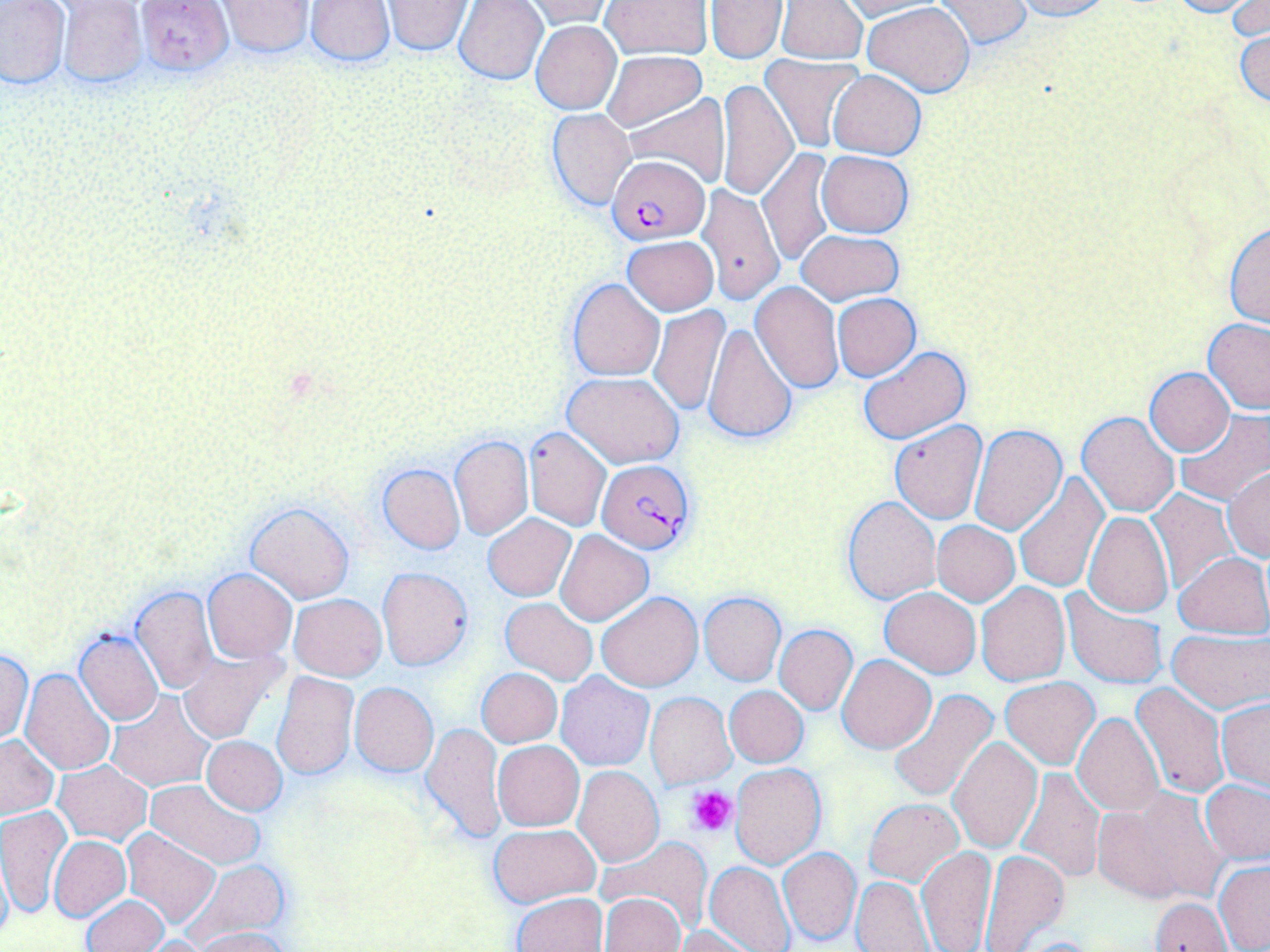
Summary:
  - Coordinate format: approximate bounding boxes as (x1,y1)-(x2,y2) corner pairs in pixels
  - Platelet locations: (688,785)-(739,837)
  - Plasmodium falciparum-infected red blood cell locations: (607,154)-(711,244), (596,458)-(697,555)
  - Uninfected red blood cell locations: (133,0)-(233,76), (304,0)-(395,67), (382,0)-(473,55), (518,0)-(615,29), (600,0)-(713,58), (706,0)-(786,63), (777,0)-(867,65), (1007,0)-(1111,21), (1165,0)-(1259,17), (1230,0)-(1269,42), (0,1)-(71,89), (57,1)-(149,88), (216,1)-(315,57), (454,1)-(549,85), (835,1)-(939,20), (932,1)-(1031,49), (861,2)-(975,96), (530,20)-(621,115), (1234,26)-(1270,108), (601,51)-(706,132), (761,55)-(865,153), (828,70)-(925,161), (717,78)-(798,201), (621,94)-(730,187), (546,108)-(636,210), (759,147)-(837,267), (816,150)-(915,238), (696,182)-(783,305), (1225,223)-(1270,328), (796,229)-(904,304), (623,236)-(718,315), (567,278)-(665,381), (751,281)-(844,392), (832,293)-(920,380), (648,306)-(729,416), (1203,318)-(1270,414), (704,322)-(797,446), (858,346)-(971,443), (1145,368)-(1234,456), (565,371)-(683,467), (1173,409)-(1270,504), (1077,410)-(1180,517), (890,420)-(987,523), (969,423)-(1068,536), (524,426)-(612,531), (450,434)-(532,540), (376,464)-(466,555), (1224,468)-(1270,560), (1013,472)-(1108,592), (1145,489)-(1237,595), (842,496)-(941,604), (246,501)-(355,603), (1083,511)-(1174,617), (483,513)-(576,601), (931,521)-(1019,606), (555,529)-(654,626), (1174,551)-(1269,638), (377,567)-(473,671), (203,568)-(297,664), (976,581)-(1071,685), (131,586)-(218,693), (879,587)-(981,677), (1060,587)-(1168,690), (597,590)-(702,691), (699,591)-(785,685), (289,594)-(387,680), (501,597)-(597,685), (774,624)-(858,714), (74,629)-(162,724), (1168,630)-(1269,710), (178,648)-(287,743), (0,649)-(32,743), (836,653)-(936,753), (20,669)-(116,776), (476,669)-(562,747), (271,670)-(358,781), (556,672)-(654,771), (1000,677)-(1100,770), (1131,680)-(1229,800), (349,683)-(438,776), (724,685)-(808,767), (889,691)-(1001,806), (106,692)-(213,792), (646,692)-(735,789), (1217,698)-(1270,792), (1072,713)-(1164,818), (422,722)-(507,845), (0,735)-(59,820), (202,735)-(287,815), (947,737)-(1042,853), (493,740)-(584,831), (54,760)-(150,845), (731,764)-(827,869), (573,765)-(664,867), (1015,767)-(1105,883), (145,779)-(266,868), (1202,780)-(1270,862), (1092,790)-(1222,902), (863,799)-(962,884), (0,807)-(71,918), (488,823)-(601,907), (121,828)-(220,927), (48,835)-(129,920), (598,836)-(714,934), (779,846)-(862,946), (916,846)-(997,952), (979,850)-(1069,952), (0,853)-(12,945), (184,858)-(291,943), (705,860)-(795,952), (1214,861)-(1270,951), (851,876)-(934,951), (513,893)-(607,952), (600,894)-(686,952), (82,896)-(168,952), (1150,897)-(1232,951), (672,925)-(759,951), (192,927)-(293,952), (135,936)-(213,952), (1011,936)-(1099,952)
  - Slide-level diagnosis: Plasmodium falciparum
  - Magnification: 1000x
  - Modality: optical microscopy
  - Field of view: single
  - Preparation: thin blood smear
  - Image size: 1270×952 pixels
  - Stain: May-Grünwald-Giemsa